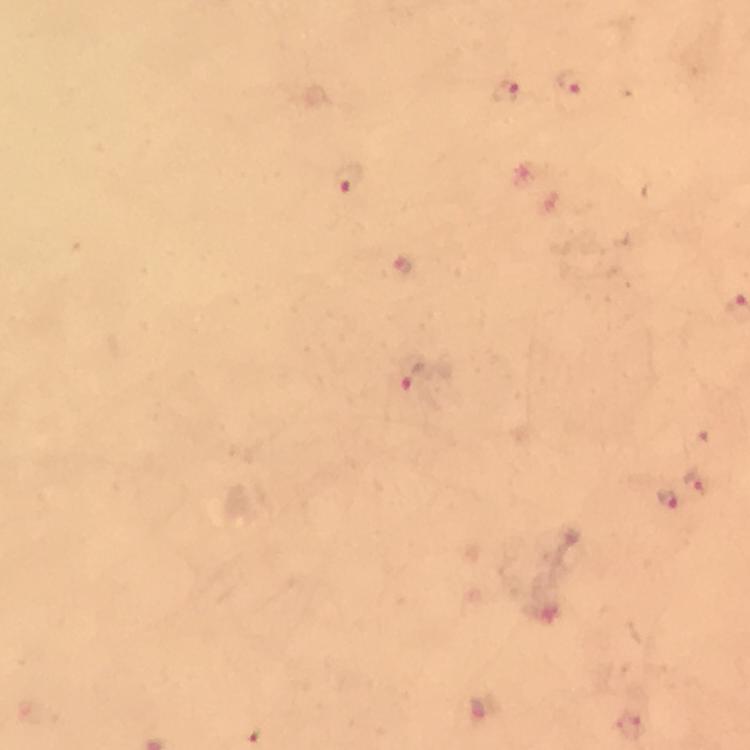

Approximate centers as (x, y) in pixels. Plasmodium parasite locations: (571, 84), (505, 91), (350, 180), (404, 267), (411, 377), (698, 482), (669, 498). Immersion oil applied. Smartphone photograph taken through a microscope. 100x magnification. Giemsa stain. Cropped region of a single field of view. From a malaria diagnostic workup. Image is 750×750 pixels. Thick blood smear.